Locate every Plasmodium parasite and every leukocyte.
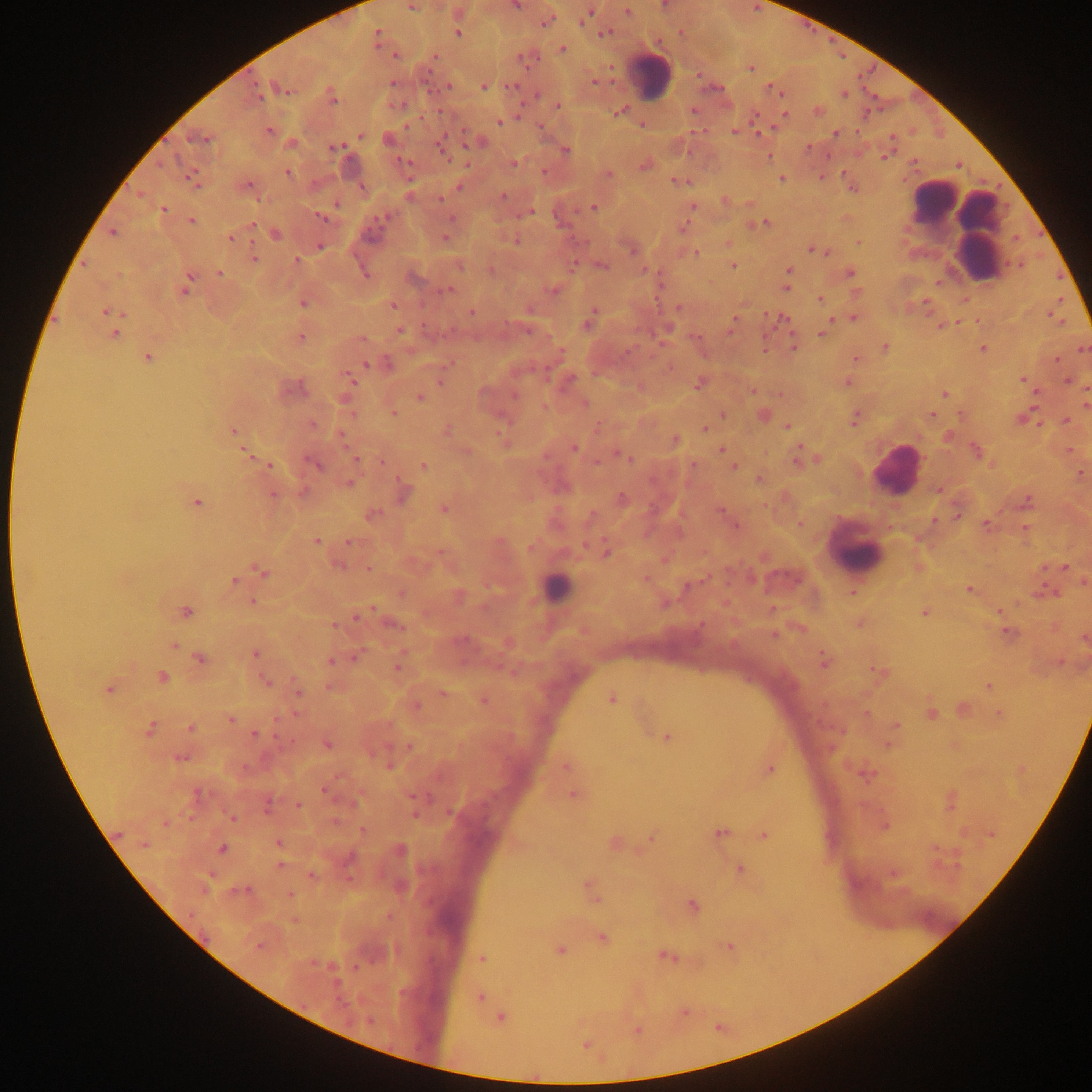

Approximate centers as x y in pixels.
Plasmodium parasites: 515 5; 411 7; 628 12; 585 16; 546 21; 458 34; 604 34; 377 36; 562 49; 395 56; 435 56; 750 68; 594 81; 393 83; 448 86; 484 87; 512 87; 284 89; 772 90; 844 94; 256 95; 537 95; 332 98; 558 106; 619 112; 785 115; 499 122; 269 130; 734 131; 835 134; 360 135; 198 138; 442 146; 335 148; 566 150; 885 156; 404 162; 513 164; 645 166; 288 172; 544 172; 609 175; 781 178; 192 179; 680 182; 247 185; 460 187; 504 196; 440 199; 337 205; 693 206; 593 207; 163 210; 530 213; 322 218; 451 220; 192 221; 765 223; 252 225; 113 233; 276 234; 231 238; 446 239; 516 241; 858 243; 320 246; 813 250; 632 251; 819 252; 697 253; 254 259; 296 260; 460 266; 602 266; 733 266; 788 271; 220 273; 365 273; 850 273; 189 278; 786 287; 185 288; 447 290; 552 290; 820 299; 925 302; 303 303; 394 305; 678 308; 105 312; 472 313; 853 318; 733 321; 587 325; 731 326; 400 331; 115 334; 822 334; 301 337; 363 340; 793 347; 885 347; 983 348; 1083 349; 147 357; 856 359; 1056 360; 366 364; 1023 380; 351 381; 1068 381; 847 382; 698 385; 944 394; 515 395; 419 397; 585 403; 394 414; 723 415; 932 416; 854 420; 1067 421; 312 423; 788 426; 704 429; 233 431; 676 440; 574 448; 721 450; 975 450; 246 453; 627 457; 797 458; 356 459; 382 462; 314 465; 423 465; 693 465; 269 466; 733 467; 1080 472; 759 478; 349 484; 938 491; 404 492; 302 493; 273 495; 623 499; 1028 502; 197 503; 443 509; 721 511; 373 515; 799 524; 987 525; 736 526; 316 541; 349 542; 606 551; 439 553; 339 566; 1065 567; 369 568; 261 572; 646 579; 234 581; 687 585; 969 590; 852 592; 401 593; 253 602; 773 608; 373 609; 186 612; 924 613; 357 618; 334 626; 395 626; 1008 632; 774 635; 173 646; 255 655; 357 656; 200 658; 331 662; 824 662; 398 668; 879 672; 162 677; 267 683; 989 687; 109 689; 299 692; 443 694; 612 698; 483 701; 932 714; 1000 714; 231 719; 897 724; 191 728; 150 729; 256 734; 666 737; 328 744; 889 745; 409 747; 181 758; 566 766; 770 770; 325 789; 573 794; 299 806; 267 807; 450 813; 232 818; 362 832; 720 833; 764 835; 652 839; 279 843; 144 845; 222 848; 280 865; 740 868; 312 875; 589 886; 246 890; 290 895; 593 896; 693 905; 602 937; 258 947; 729 947; 560 950; 666 957; 483 958; 480 997; 684 1012; 501 1019; 637 1030; 586 1045.
Leukocytes: 653 76; 932 200; 963 219; 896 470; 856 554; 556 587.

preparation = thick blood smear
capture = mobile-phone photograph through a microscope
image size = 1092×1092 pixels
field of view = single
country = Ghana